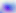
400x magnification. Micrograph. Toxoplasma gondii is shown.